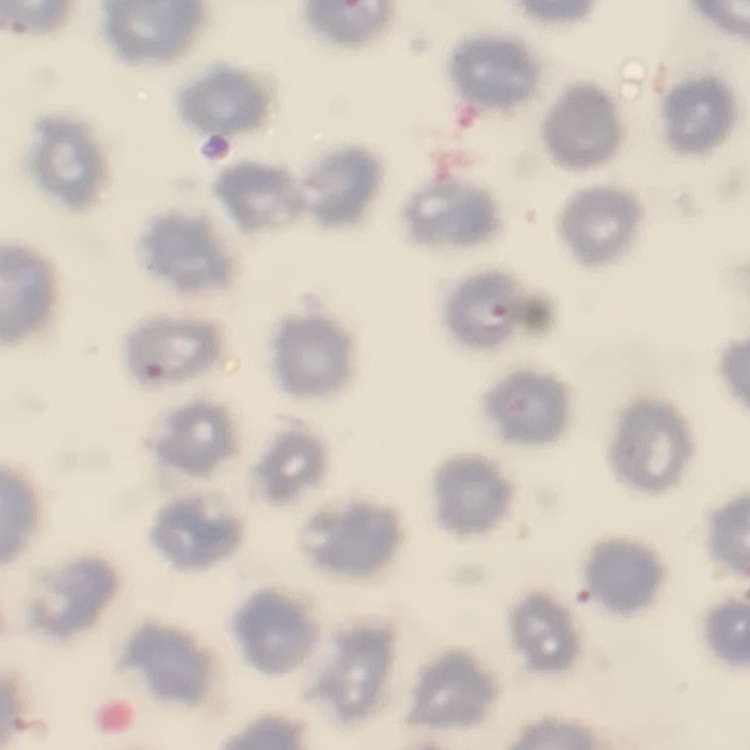
The erythrocytes show no rouleaux formation. Thin peripheral smear. Square crop of a larger photomicrograph. Field's or Giemsa stain.